Report the malaria status of this cell.
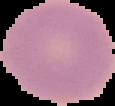

Uninfected.

image_type: cell region segmented out of the field of view; surrounding area masked to black
image_size: 115×106 pixels
preparation: thin blood film